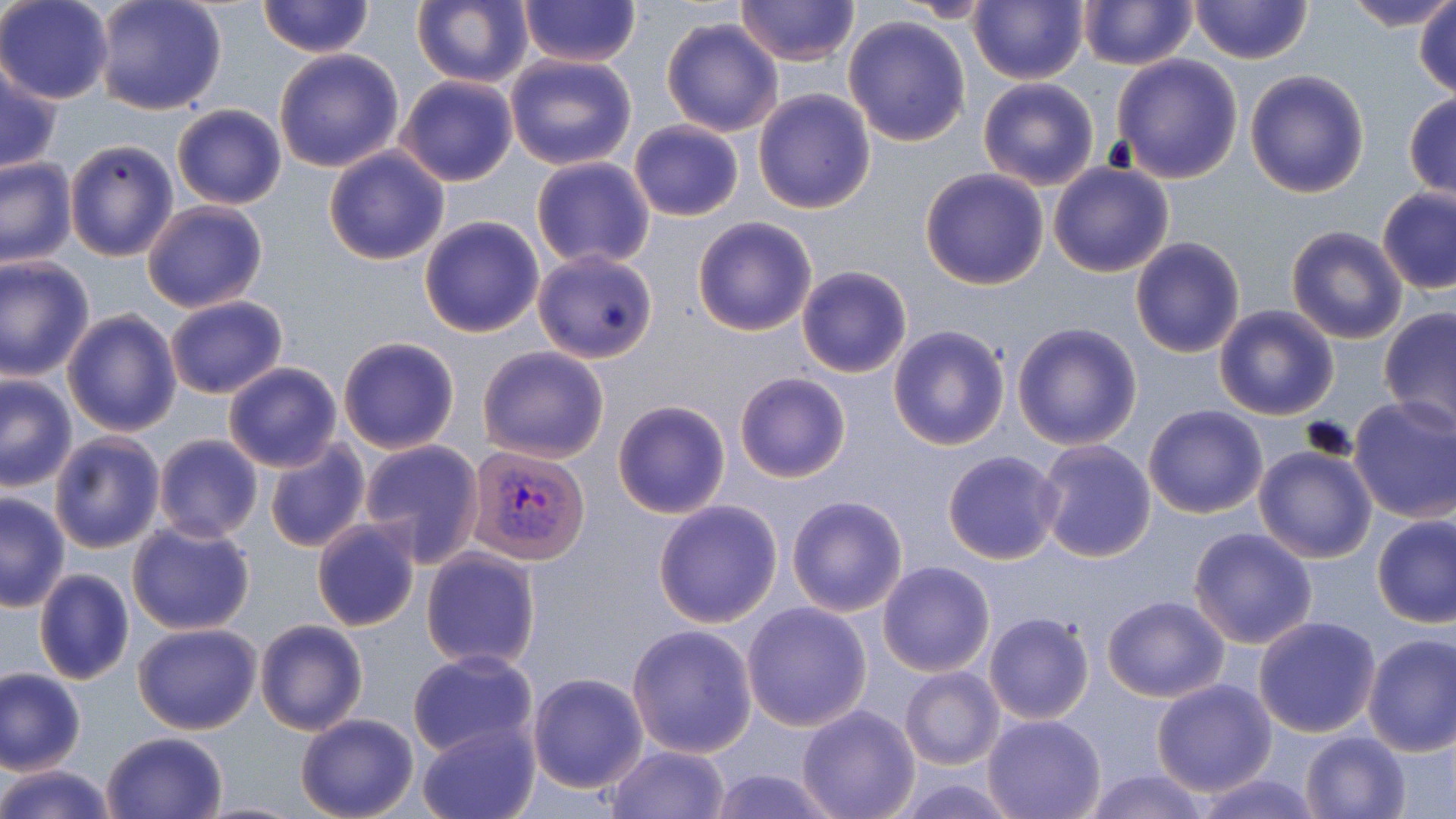
slide-level diagnosis = Plasmodium vivax
image size = 1456×819 pixels
field of view = one of a larger specimen
uninfected red blood cell locations = approximate bounding boxes as named x1/y1/x2/y2 corners in pixels: (x1=1, y1=0, x2=113, y2=104), (x1=91, y1=0, x2=229, y2=117), (x1=517, y1=0, x2=641, y2=67), (x1=735, y1=0, x2=859, y2=66), (x1=969, y1=0, x2=1089, y2=85), (x1=1339, y1=0, x2=1456, y2=32), (x1=256, y1=1, x2=374, y2=58), (x1=410, y1=1, x2=534, y2=88), (x1=894, y1=1, x2=1003, y2=22), (x1=1077, y1=1, x2=1197, y2=70), (x1=1187, y1=1, x2=1313, y2=65), (x1=1413, y1=3, x2=1456, y2=100), (x1=842, y1=13, x2=971, y2=146), (x1=660, y1=17, x2=785, y2=138), (x1=273, y1=48, x2=404, y2=173), (x1=504, y1=53, x2=637, y2=170), (x1=794, y1=53, x2=970, y2=192), (x1=1111, y1=53, x2=1244, y2=182), (x1=1, y1=56, x2=64, y2=173), (x1=1243, y1=68, x2=1370, y2=198), (x1=396, y1=74, x2=519, y2=186), (x1=978, y1=76, x2=1100, y2=191), (x1=752, y1=89, x2=875, y2=214), (x1=1404, y1=91, x2=1456, y2=202), (x1=172, y1=103, x2=286, y2=209), (x1=629, y1=120, x2=744, y2=222), (x1=62, y1=137, x2=179, y2=262), (x1=323, y1=146, x2=450, y2=267), (x1=0, y1=157, x2=76, y2=268), (x1=531, y1=157, x2=654, y2=270), (x1=1048, y1=162, x2=1175, y2=278), (x1=919, y1=166, x2=1048, y2=289), (x1=1376, y1=187, x2=1456, y2=293), (x1=141, y1=200, x2=268, y2=313), (x1=418, y1=216, x2=545, y2=337), (x1=692, y1=217, x2=817, y2=336), (x1=1286, y1=226, x2=1408, y2=344), (x1=1130, y1=237, x2=1246, y2=358), (x1=533, y1=249, x2=659, y2=364), (x1=0, y1=256, x2=96, y2=380), (x1=797, y1=266, x2=912, y2=378), (x1=164, y1=295, x2=287, y2=400), (x1=1213, y1=304, x2=1340, y2=421), (x1=1379, y1=306, x2=1456, y2=433), (x1=60, y1=307, x2=183, y2=436), (x1=1012, y1=322, x2=1143, y2=451), (x1=887, y1=325, x2=1011, y2=450), (x1=337, y1=335, x2=461, y2=454), (x1=476, y1=345, x2=610, y2=463), (x1=223, y1=361, x2=343, y2=472), (x1=735, y1=371, x2=851, y2=483), (x1=0, y1=372, x2=76, y2=491), (x1=1349, y1=395, x2=1455, y2=524), (x1=611, y1=399, x2=731, y2=519), (x1=1143, y1=405, x2=1269, y2=517), (x1=46, y1=430, x2=166, y2=554), (x1=153, y1=433, x2=264, y2=543), (x1=263, y1=435, x2=371, y2=554), (x1=359, y1=439, x2=484, y2=566), (x1=1035, y1=439, x2=1157, y2=563), (x1=1253, y1=446, x2=1377, y2=563), (x1=943, y1=451, x2=1065, y2=565), (x1=0, y1=490, x2=71, y2=611), (x1=787, y1=494, x2=908, y2=617), (x1=653, y1=500, x2=784, y2=628), (x1=1371, y1=514, x2=1456, y2=628), (x1=312, y1=518, x2=421, y2=632), (x1=126, y1=519, x2=256, y2=637), (x1=1188, y1=525, x2=1319, y2=649), (x1=420, y1=548, x2=542, y2=670), (x1=878, y1=560, x2=995, y2=677), (x1=33, y1=568, x2=135, y2=686), (x1=1102, y1=594, x2=1229, y2=703), (x1=741, y1=602, x2=873, y2=732), (x1=983, y1=610, x2=1094, y2=725), (x1=1252, y1=616, x2=1382, y2=738), (x1=256, y1=618, x2=368, y2=736), (x1=133, y1=622, x2=262, y2=734), (x1=627, y1=624, x2=758, y2=758), (x1=1362, y1=633, x2=1456, y2=756), (x1=406, y1=650, x2=540, y2=760), (x1=900, y1=666, x2=1004, y2=769), (x1=0, y1=669, x2=87, y2=776), (x1=527, y1=672, x2=649, y2=793), (x1=1150, y1=679, x2=1277, y2=798), (x1=795, y1=705, x2=920, y2=819), (x1=295, y1=713, x2=419, y2=819), (x1=982, y1=714, x2=1106, y2=819), (x1=419, y1=721, x2=541, y2=818), (x1=1300, y1=730, x2=1413, y2=818), (x1=101, y1=731, x2=228, y2=818), (x1=604, y1=744, x2=732, y2=819), (x1=0, y1=765, x2=117, y2=819), (x1=705, y1=766, x2=843, y2=819), (x1=1081, y1=770, x2=1211, y2=819), (x1=1186, y1=773, x2=1329, y2=818)
magnification = 1000x
Plasmodium vivax-infected red blood cell locations = approximate bounding boxes as named x1/y1/x2/y2 corners in pixels: (x1=468, y1=444, x2=588, y2=565)
stain = May-Grünwald-Giemsa
modality = light microscopy
preparation = thin blood smear